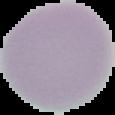

image type = cell region segmented out of the field of view; surrounding area masked to black
preparation = thin blood film
result = no malaria parasites detected
image size = 115×115 pixels